Point out each Plasmodium parasite and each leukocyte.
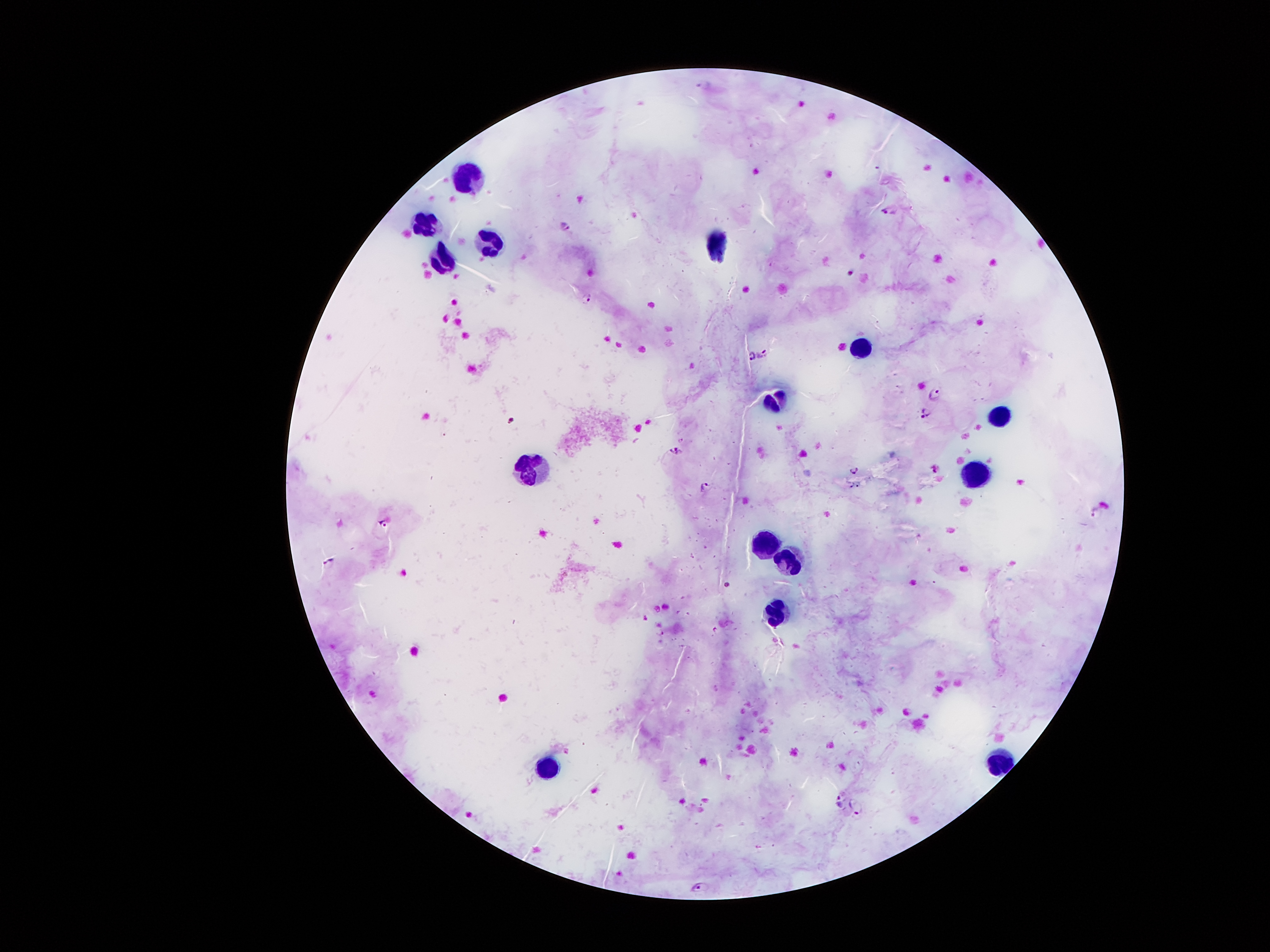
Approximate centers as [x, y] in pixels.
Plasmodium parasites: [887, 210], [567, 227], [586, 299], [760, 352], [750, 356], [934, 395], [926, 411], [671, 447], [679, 452], [852, 467], [937, 467], [704, 486], [1093, 510], [384, 522], [327, 561], [662, 631], [838, 799], [857, 807], [702, 887].
Leukocytes: [468, 176], [424, 225], [490, 243], [722, 243], [442, 259], [864, 346], [774, 398], [998, 417], [535, 468], [976, 477], [765, 545], [790, 561], [778, 613], [1001, 760], [546, 765].

Summary:
  - Patient malaria status: positive for Plasmodium falciparum
  - Capture: smartphone through the microscope eyepiece
  - Preparation: thick peripheral-blood smear
  - Image size: 1270×952 pixels
  - Magnification: 100x
  - Stain: Giemsa
  - Field of view: one from this slide